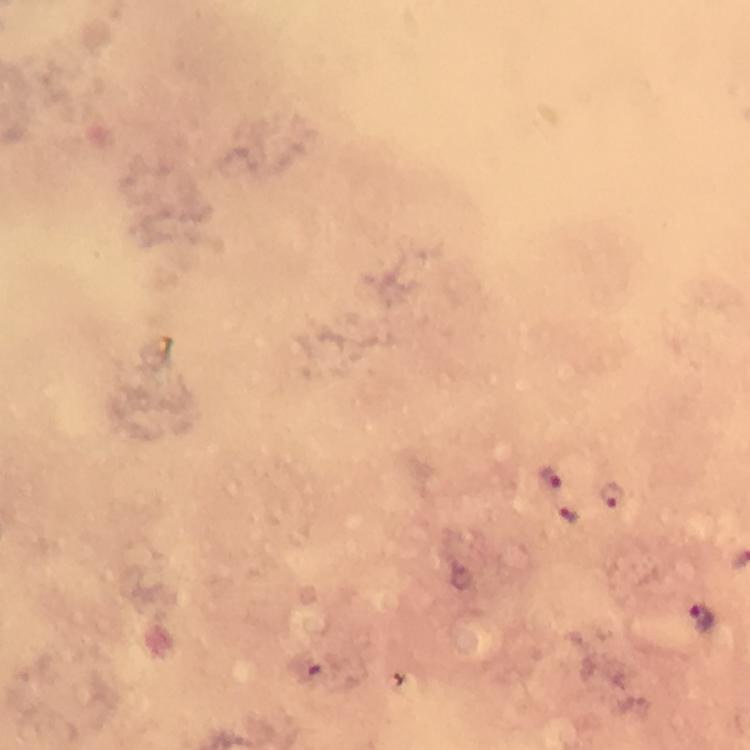

Approximate centers as {x, y} in pixels. Malaria parasite locations: {551, 479}, {610, 493}, {566, 515}, {701, 617}. Immersion oil was used. 100x magnification. Photographed through the microscope with a smartphone camera. From a diagnostic examination for malaria. Giemsa-stained preparation. Cropped region of a single field of view. Thick blood smear. Image is 750×750 pixels.